Give the extent of all uninfected red blood cells.
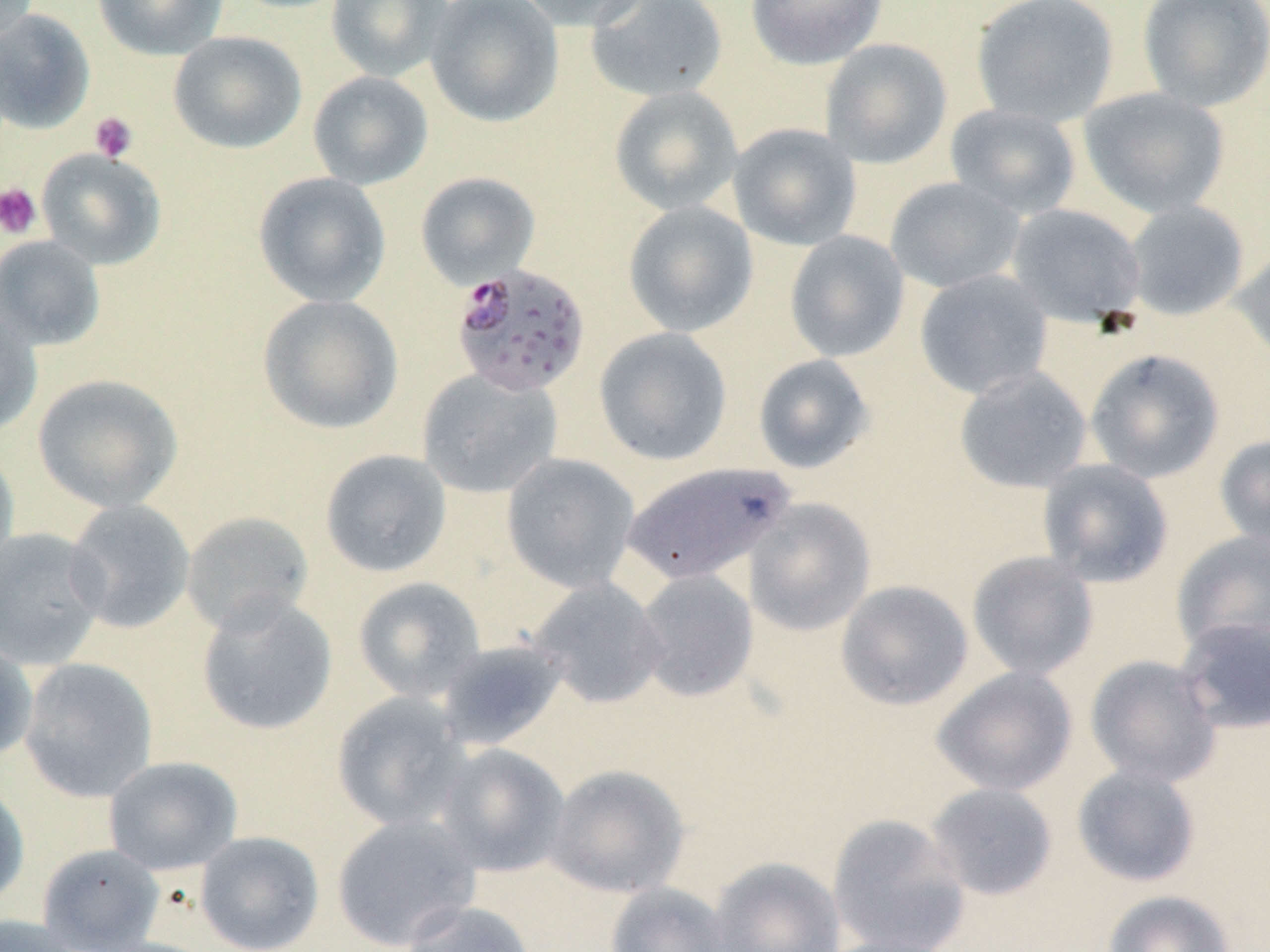
Approximate bounding boxes as (x1, y1, x2, y2) in pixels.
Uninfected red blood cells: (92, 0, 229, 60), (325, 0, 453, 82), (425, 0, 564, 128), (513, 0, 651, 32), (745, 0, 887, 70), (971, 0, 1119, 126), (1136, 0, 1270, 112), (0, 1, 39, 49), (585, 1, 728, 102), (0, 8, 95, 134), (168, 31, 306, 154), (819, 38, 952, 169), (307, 71, 433, 190), (609, 85, 743, 216), (1077, 87, 1231, 219), (944, 103, 1082, 219), (727, 123, 862, 251), (36, 148, 166, 270), (415, 171, 541, 288), (253, 172, 391, 307), (885, 177, 1026, 294), (1123, 200, 1250, 321), (623, 201, 758, 337), (1006, 204, 1146, 327), (784, 231, 910, 362), (0, 235, 106, 351), (1232, 245, 1270, 365), (914, 269, 1054, 400), (257, 294, 404, 435), (0, 307, 43, 438), (594, 327, 733, 466), (1084, 348, 1225, 484), (752, 353, 875, 474), (953, 366, 1093, 494), (417, 368, 561, 499), (32, 373, 183, 513), (1214, 434, 1270, 550), (0, 445, 20, 580), (319, 449, 452, 578), (501, 453, 640, 593), (1037, 458, 1174, 588), (621, 460, 796, 587), (743, 497, 877, 636), (63, 499, 196, 634), (181, 511, 315, 636), (0, 527, 109, 669), (1171, 529, 1270, 656), (966, 550, 1100, 681), (633, 569, 759, 703), (352, 576, 485, 702), (527, 578, 667, 709), (835, 580, 974, 711), (195, 595, 338, 736), (1175, 616, 1270, 735), (0, 636, 38, 762), (435, 638, 569, 751), (1084, 654, 1223, 788), (18, 657, 159, 803), (931, 666, 1078, 797), (331, 691, 471, 831), (433, 743, 570, 878), (103, 755, 243, 875), (546, 764, 690, 899), (1071, 764, 1202, 887), (0, 779, 30, 910), (924, 782, 1058, 901), (331, 813, 481, 951), (827, 813, 971, 952), (195, 831, 324, 951), (37, 843, 165, 951), (707, 857, 846, 952), (605, 883, 733, 952), (1101, 890, 1236, 952), (399, 899, 539, 952), (0, 914, 85, 952), (816, 934, 959, 952).

Summary:
  - Plasmodium falciparum-infected red blood cell locations: (450, 263, 591, 397)
  - Platelet locations: (89, 111, 138, 163), (0, 183, 42, 239)
  - Slide-level diagnosis: Plasmodium falciparum
  - Field of view: one of a larger specimen
  - Magnification: 1000x
  - Stain: May-Grünwald-Giemsa
  - Preparation: thin blood film
  - Modality: optical microscopy
  - Image size: 1270×952 pixels